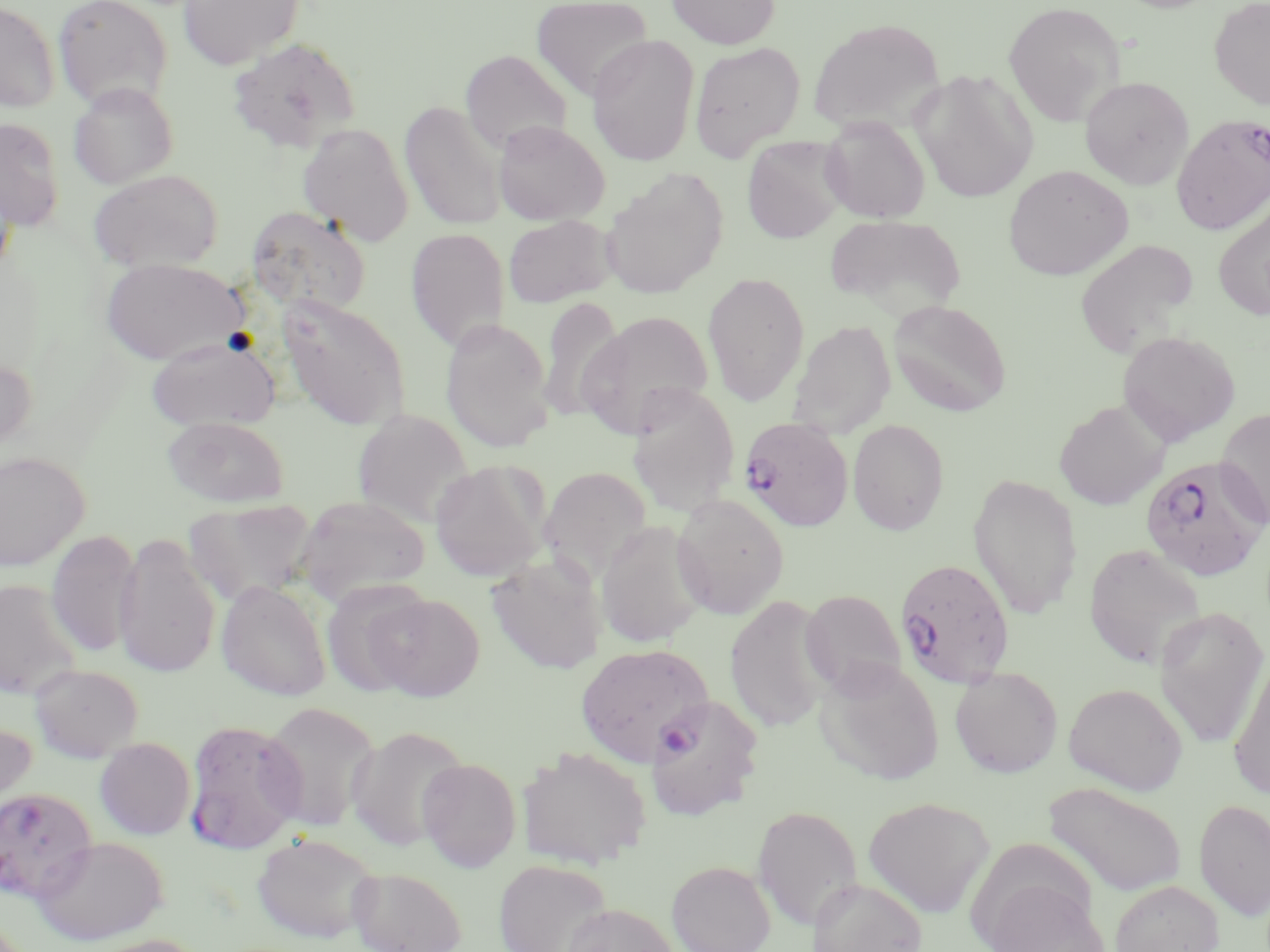

Summary:
  - Coordinate format: approximate bounding boxes as [x1, y1, x2, y2] in pixels
  - Plasmodium falciparum-infected red blood cell locations: [1171, 115, 1270, 234], [736, 417, 851, 534], [1139, 455, 1269, 582], [894, 557, 1015, 688], [574, 642, 715, 766], [182, 718, 306, 854], [0, 787, 97, 902]
  - Uninfected red blood cell locations: [53, 0, 174, 111], [177, 0, 304, 69], [531, 0, 655, 100], [666, 0, 780, 49], [1209, 0, 1270, 109], [0, 1, 61, 113], [1003, 1, 1126, 127], [807, 17, 945, 134], [587, 34, 700, 166], [227, 38, 362, 153], [689, 41, 805, 162], [460, 49, 573, 155], [910, 69, 1038, 203], [1080, 76, 1194, 189], [68, 82, 178, 189], [400, 100, 506, 232], [819, 115, 932, 222], [0, 117, 65, 232], [492, 120, 610, 226], [297, 123, 414, 247], [742, 136, 848, 244], [1003, 164, 1134, 280], [600, 167, 730, 298], [88, 169, 224, 272], [0, 177, 17, 280], [1213, 202, 1270, 322], [246, 206, 371, 316], [503, 214, 616, 307], [405, 227, 511, 350], [1075, 238, 1199, 358], [100, 257, 248, 365], [702, 271, 810, 406], [277, 294, 411, 430], [537, 295, 625, 423], [889, 300, 1012, 416], [578, 310, 715, 438], [440, 317, 555, 453], [787, 320, 896, 438], [1117, 330, 1240, 445], [146, 335, 281, 432], [0, 354, 38, 456], [626, 384, 740, 517], [1054, 400, 1168, 510], [1216, 407, 1270, 528], [351, 409, 475, 528], [163, 416, 290, 508], [847, 419, 950, 535], [0, 451, 90, 571], [430, 460, 550, 582], [539, 466, 654, 584], [967, 472, 1083, 620], [671, 493, 789, 620], [293, 495, 432, 604], [184, 499, 318, 609], [595, 520, 709, 649], [47, 529, 141, 658], [114, 534, 221, 678], [1083, 543, 1206, 669], [486, 551, 609, 675], [321, 578, 433, 696], [0, 579, 83, 699], [216, 579, 332, 701], [800, 589, 906, 698], [366, 593, 485, 702], [724, 594, 834, 732], [1153, 605, 1269, 748], [1228, 652, 1270, 802], [814, 657, 945, 785], [29, 662, 144, 762], [949, 666, 1063, 778], [1063, 682, 1187, 795], [644, 695, 764, 819], [260, 701, 380, 832], [0, 721, 36, 825], [346, 725, 470, 851], [95, 737, 195, 840], [516, 747, 652, 869], [417, 757, 522, 871], [1045, 782, 1186, 897], [863, 795, 995, 918], [1194, 797, 1270, 922], [752, 805, 863, 930], [252, 832, 380, 943], [33, 835, 169, 944], [494, 859, 612, 952], [667, 860, 775, 952], [348, 866, 467, 952], [807, 877, 928, 952], [978, 878, 1109, 952], [1111, 880, 1223, 952], [561, 903, 679, 952], [81, 934, 210, 952]
  - Slide-level diagnosis: Plasmodium falciparum
  - Modality: light microscopy
  - Image size: 1270×952 pixels
  - Field of view: single
  - Preparation: thin blood smear
  - Stain: May-Grünwald-Giemsa
  - Magnification: 1000x